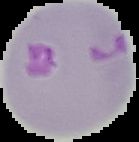
malaria status = parasitized
image size = 139×142 pixels
preparation = thin blood smear
image type = segmented cell region with the area outside set to black